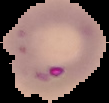
Summary:
  - Image type: segmented cell region on a black background
  - Result: malaria parasites identified
  - Preparation: thin blood film
  - Image size: 109×103 pixels